Name the cell type shown.
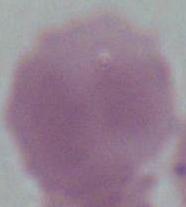
An erythrocyte.

{
  "modality": "photomicrograph",
  "magnification": "1000x"
}